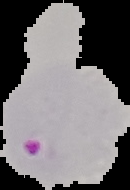 The area outside the segmented cell region is set to black. From a thin blood smear. Malaria status: parasitized. Image is 130×190 pixels.